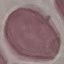
Summary:
  - Malaria status: uninfected
  - Capture: smartphone through the microscope eyepiece
  - Preparation: thin smear
  - Image type: cell patch, automatically extracted from a larger field of view and resized to 64 × 64 pixels
  - Stain: Giemsa